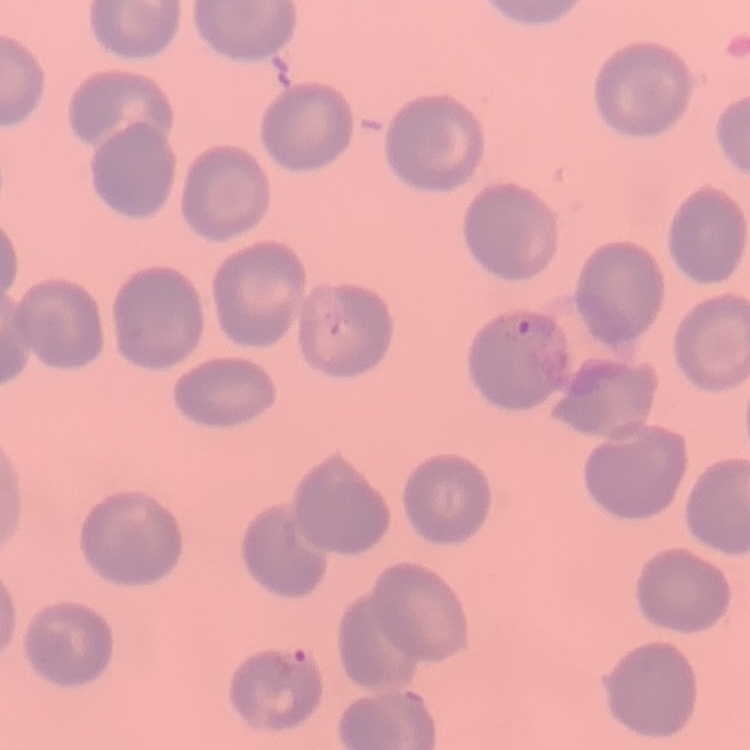

Summary:
  - Red blood cell morphology: no rouleaux formation
  - Preparation: thin blood smear
  - Image type: square crop of a larger photomicrograph
  - Stain: Field's or Giemsa